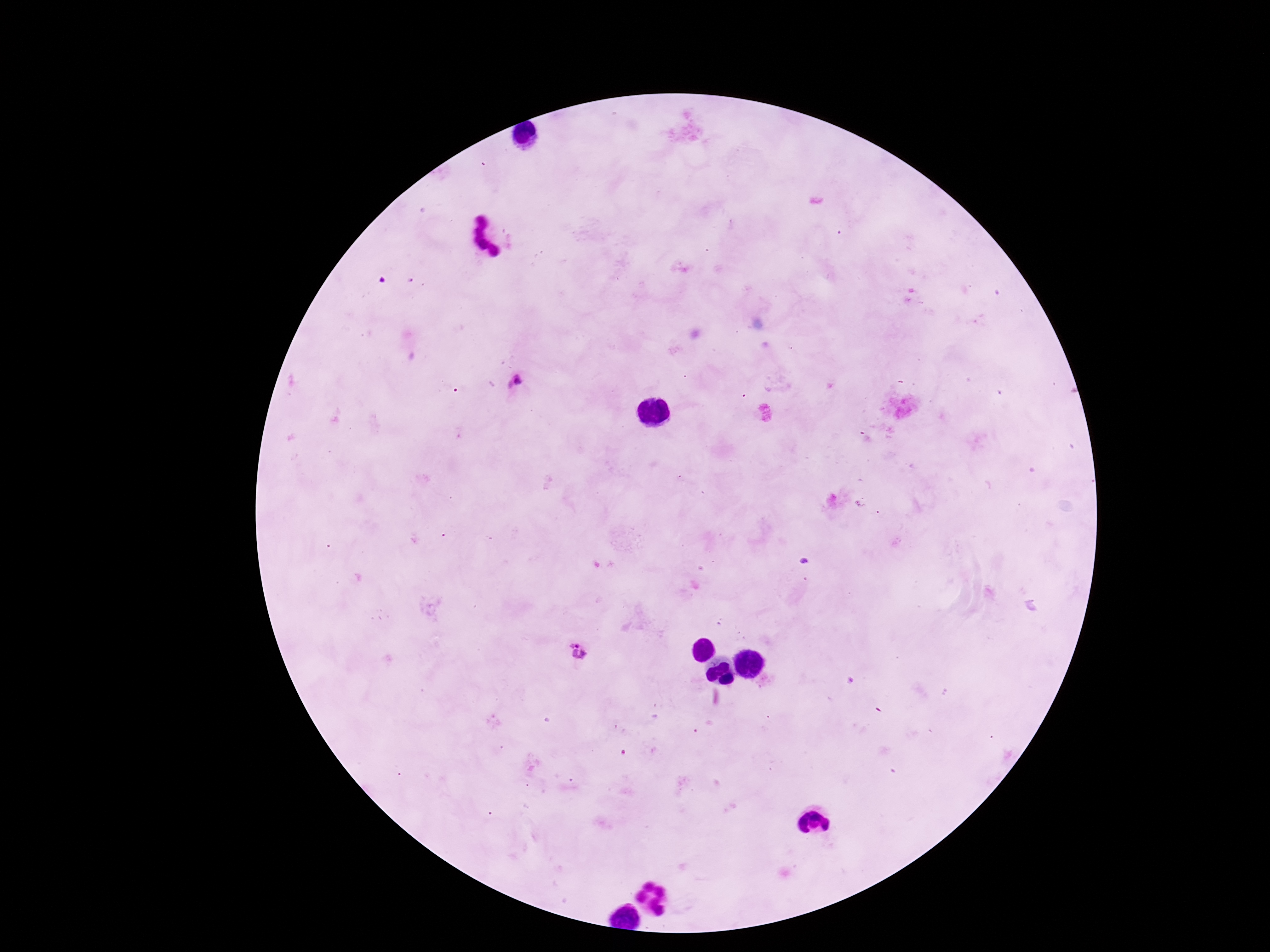

Approximate centers as {x, y} in pixels.
Summary:
  - Plasmodium parasite locations: {517, 380}, {579, 652}
  - Stain: Giemsa
  - Patient malaria status: infected
  - Image size: 1270×952 pixels
  - Field of view: one from this slide
  - Magnification: 100x
  - Preparation: thick peripheral-blood smear
  - Capture: smartphone camera through the microscope eyepiece